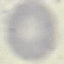
Malaria status: uninfected. Cell patch, automatically extracted from a larger field of view and resized to 64 × 64 pixels. Giemsa-stained preparation. Thin smear of blood. Photographed with a smartphone camera at the microscope eyepiece.